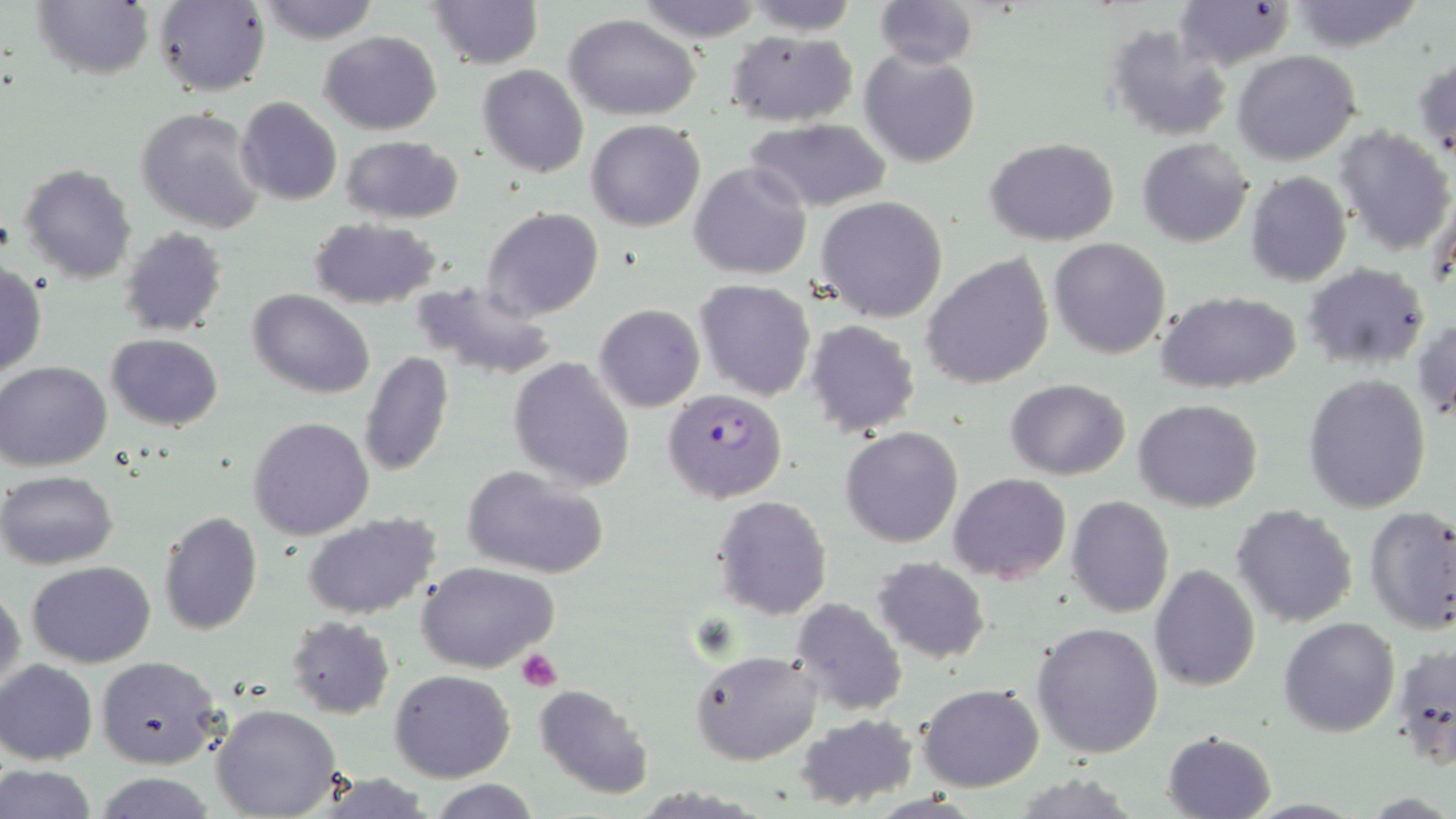

Summary:
  - Coordinate format: approximate bounding boxes as (x1, y1, x2, y2) in pixels
  - Platelet locations: (516, 649, 563, 691)
  - Plasmodium falciparum-infected red blood cell locations: (662, 389, 789, 502)
  - Uninfected red blood cell locations: (874, 0, 978, 69), (1288, 0, 1426, 51), (29, 1, 153, 82), (153, 1, 270, 97), (253, 1, 384, 45), (427, 1, 542, 70), (632, 1, 768, 44), (743, 1, 859, 36), (1176, 3, 1293, 71), (564, 14, 700, 120), (1105, 25, 1234, 143), (726, 30, 857, 125), (318, 31, 442, 134), (859, 47, 981, 168), (1233, 50, 1361, 166), (1413, 51, 1456, 161), (478, 64, 588, 178), (234, 96, 343, 206), (135, 107, 266, 234), (587, 119, 706, 232), (747, 119, 893, 212), (1335, 126, 1455, 256), (340, 136, 465, 224), (984, 137, 1121, 244), (1137, 138, 1255, 247), (690, 161, 812, 281), (20, 164, 138, 282), (1245, 171, 1351, 287), (1429, 183, 1456, 296), (817, 196, 948, 323), (481, 207, 603, 321), (308, 217, 442, 309), (120, 228, 228, 337), (1048, 237, 1171, 359), (924, 254, 1055, 391), (1304, 263, 1429, 370), (0, 264, 48, 379), (409, 279, 561, 382), (694, 279, 816, 400), (249, 289, 373, 398), (1154, 290, 1303, 394), (594, 304, 705, 412), (1413, 316, 1456, 424), (804, 320, 920, 437), (106, 334, 225, 431), (360, 351, 454, 477), (507, 357, 636, 492), (1, 360, 114, 470), (1303, 374, 1432, 514), (1005, 379, 1130, 479), (1133, 399, 1264, 513), (248, 416, 376, 540), (841, 426, 964, 548), (462, 463, 609, 579), (0, 470, 118, 569), (949, 473, 1071, 584), (712, 495, 833, 620), (1066, 496, 1176, 619), (1231, 504, 1359, 628), (1365, 506, 1456, 633), (301, 511, 443, 621), (158, 512, 262, 637), (872, 557, 990, 664), (27, 560, 155, 668), (419, 563, 559, 674), (1149, 564, 1260, 692), (0, 584, 24, 700), (790, 598, 907, 716), (287, 616, 395, 718), (1280, 617, 1400, 736), (1032, 621, 1165, 759), (1391, 641, 1455, 768), (691, 649, 822, 765), (98, 656, 223, 772), (1, 660, 98, 765), (391, 669, 514, 782), (917, 683, 1046, 792), (533, 684, 654, 799), (211, 703, 341, 817), (795, 713, 920, 811), (1163, 730, 1276, 818), (0, 764, 99, 819), (94, 774, 218, 818), (429, 779, 541, 818)
  - Slide-level diagnosis: Plasmodium falciparum
  - Preparation: thin blood smear
  - Modality: optical microscopy
  - Field of view: single
  - Magnification: 1000x
  - Image size: 1456×819 pixels
  - Stain: May-Grünwald-Giemsa